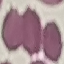

Result: no malaria parasites seen. Automatically extracted cell patch, resized to 64 × 64 pixels. Acquired by smartphone through the microscope eyepiece. Giemsa stain. Thin smear of blood.